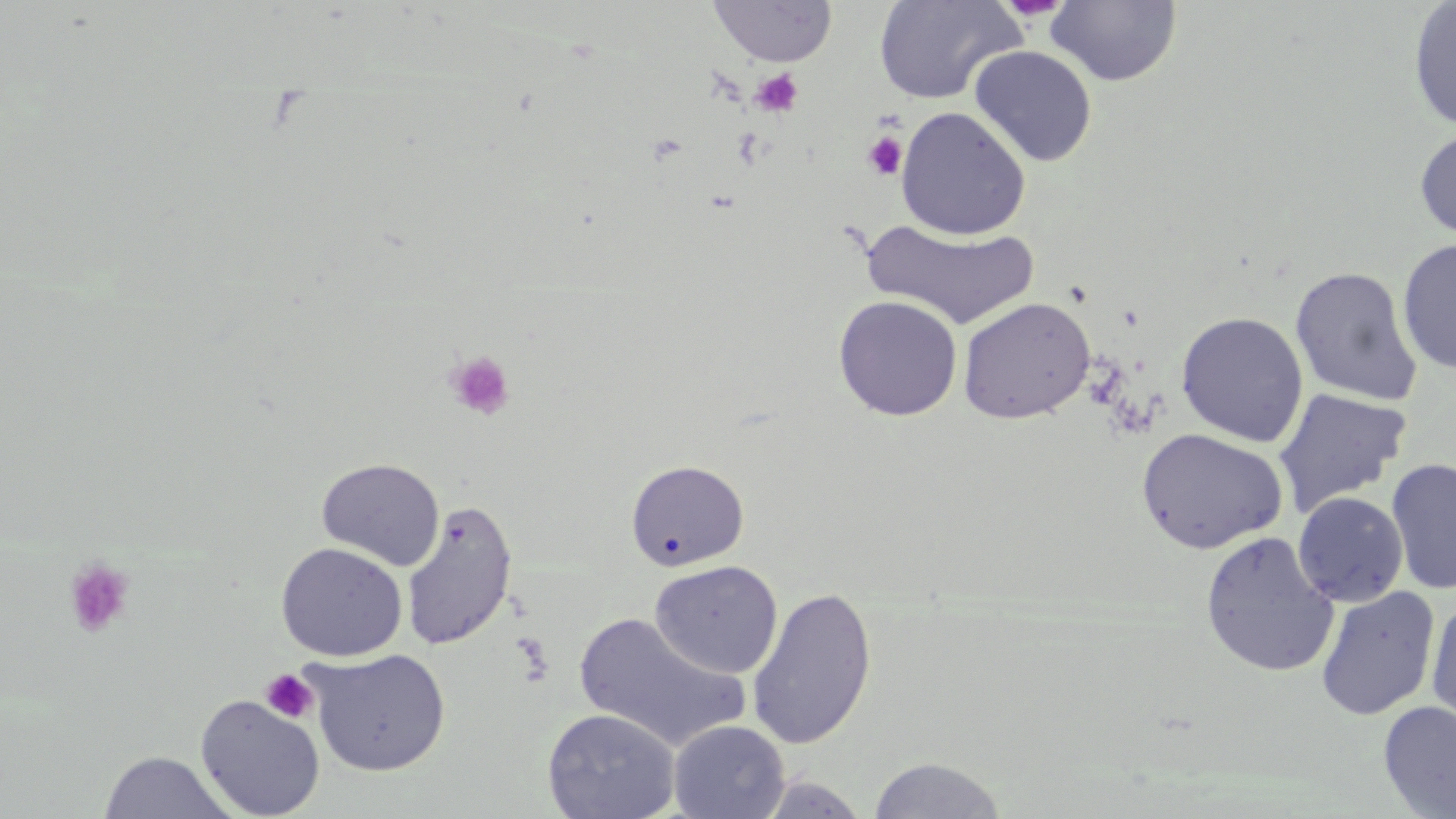

Summary:
  - Coordinate format: approximate bounding boxes as [x1, y1, x2, y2] in pixels
  - Platelet locations: [749, 68, 803, 117], [861, 131, 908, 181], [445, 350, 516, 421], [64, 557, 135, 638], [260, 669, 319, 724]
  - Uninfected red blood cell locations: [707, 0, 838, 67], [873, 0, 1023, 105], [1045, 1, 1182, 86], [1407, 2, 1456, 130], [969, 45, 1098, 167], [895, 106, 1031, 240], [1414, 124, 1456, 242], [860, 218, 1041, 330], [1397, 237, 1456, 374], [1290, 266, 1422, 406], [833, 295, 963, 421], [958, 297, 1095, 423], [1175, 311, 1309, 447], [1272, 386, 1413, 519], [1135, 428, 1289, 554], [316, 457, 445, 571], [1386, 457, 1456, 595], [626, 459, 749, 571], [1293, 491, 1408, 607], [400, 500, 518, 651], [1199, 531, 1339, 679], [275, 542, 407, 661], [650, 560, 783, 678], [746, 585, 878, 751], [1315, 586, 1440, 721], [1425, 594, 1456, 737], [573, 611, 750, 752], [304, 648, 451, 776], [195, 695, 325, 817], [1378, 700, 1456, 818], [542, 707, 681, 819], [668, 720, 790, 819], [97, 750, 238, 819], [867, 756, 1007, 818], [751, 775, 871, 818]
  - Slide-level diagnosis: no evidence of blood parasites
  - Magnification: 1000x
  - Image size: 1456×819 pixels
  - Preparation: thin blood film
  - Modality: light microscopy
  - Field of view: single
  - Stain: May-Grünwald-Giemsa